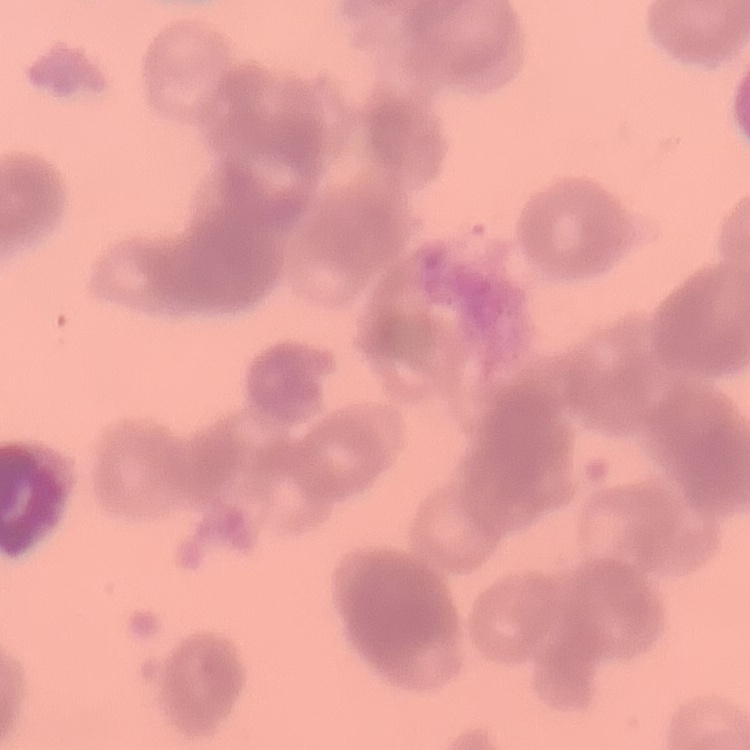

erythrocyte morphology = rouleaux formation
image type = square crop of a larger photomicrograph
preparation = thin blood film
stain = Field's or Giemsa